Assess this cell for malaria.
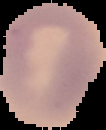
Uninfected.

image size = 106×130 pixels
preparation = thin blood film
image type = cell region segmented out of the field of view; surrounding area masked to black